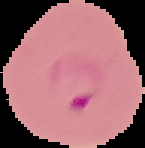
Malaria status: parasitized. Segmented cell region on a black background. Image is 145×148 pixels. From a thin blood film.